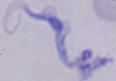
1000x magnification. Photomicrograph. A trypanosome is shown.